State which parasite is depicted.
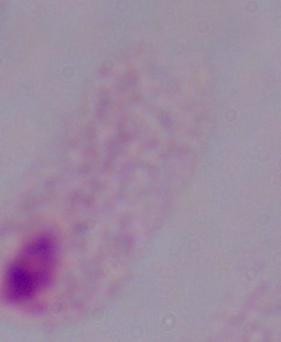

A trichomonad.

magnification = 1000x
modality = micrograph